Locate and identify every blood parasite.
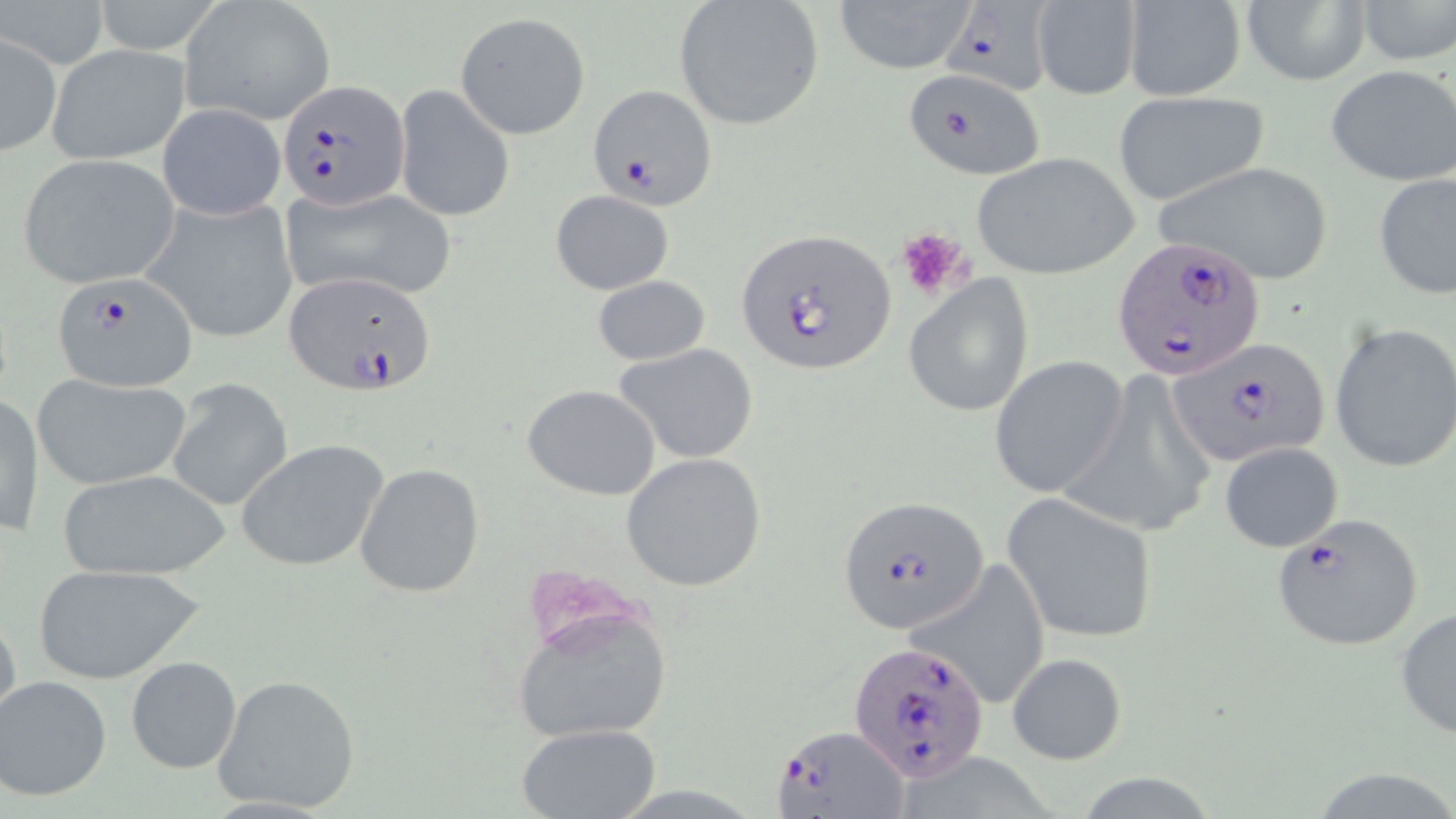

Approximate bounding boxes as [x1, y1, x2, y2] in pixels.
Plasmodium falciparum-infected red blood cells: [941, 0, 1060, 100], [902, 68, 1044, 180], [279, 79, 410, 210], [589, 84, 716, 211], [737, 227, 896, 376], [1111, 233, 1267, 383], [53, 270, 198, 392], [282, 270, 434, 395], [1170, 336, 1332, 469], [836, 495, 988, 635], [1267, 511, 1424, 652], [849, 639, 988, 783], [776, 724, 908, 817].
No Plasmodium ovale, Plasmodium malariae, Plasmodium vivax, Babesia divergens, or Trypanosoma brucei observed.

Summary:
  - Platelet locations: [894, 225, 973, 301]
  - Uninfected red blood cell locations: [2, 0, 108, 69], [93, 0, 228, 55], [181, 0, 335, 125], [830, 0, 976, 74], [672, 1, 826, 130], [1030, 1, 1143, 99], [1121, 1, 1247, 101], [1241, 1, 1368, 86], [1354, 1, 1455, 68], [454, 12, 591, 138], [1, 30, 61, 158], [46, 45, 190, 165], [1324, 64, 1456, 188], [393, 84, 514, 223], [1111, 89, 1271, 208], [157, 102, 288, 221], [970, 151, 1139, 280], [15, 154, 182, 289], [1156, 160, 1336, 287], [1374, 173, 1456, 300], [278, 184, 458, 303], [549, 189, 674, 295], [142, 197, 298, 343], [904, 274, 1036, 417], [592, 275, 710, 367], [1329, 322, 1456, 474], [613, 343, 760, 464], [990, 355, 1128, 499], [32, 373, 192, 490], [167, 380, 291, 512], [522, 384, 662, 498], [1, 393, 43, 539], [238, 439, 389, 574], [1217, 442, 1345, 551], [622, 453, 768, 592], [355, 461, 486, 598], [56, 468, 231, 580], [1002, 491, 1158, 641], [906, 558, 1053, 707], [31, 562, 205, 684], [0, 603, 21, 742], [507, 603, 674, 744], [1395, 608, 1456, 742], [1004, 653, 1128, 763], [126, 655, 242, 774], [211, 673, 362, 814], [2, 675, 112, 802], [515, 723, 666, 817], [1304, 765, 1456, 819]
  - Slide-level diagnosis: Plasmodium falciparum
  - Field of view: single
  - Stain: May-Grünwald-Giemsa
  - Image size: 1456×819 pixels
  - Modality: optical microscopy
  - Preparation: thin blood film
  - Magnification: 1000x